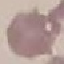

Malaria status: uninfected. Thin blood smear. Automatically extracted cell patch, resized to 64 × 64 pixels. Photographed with a smartphone camera at the microscope eyepiece. Giemsa stain.